Locate every Plasmodium parasite.
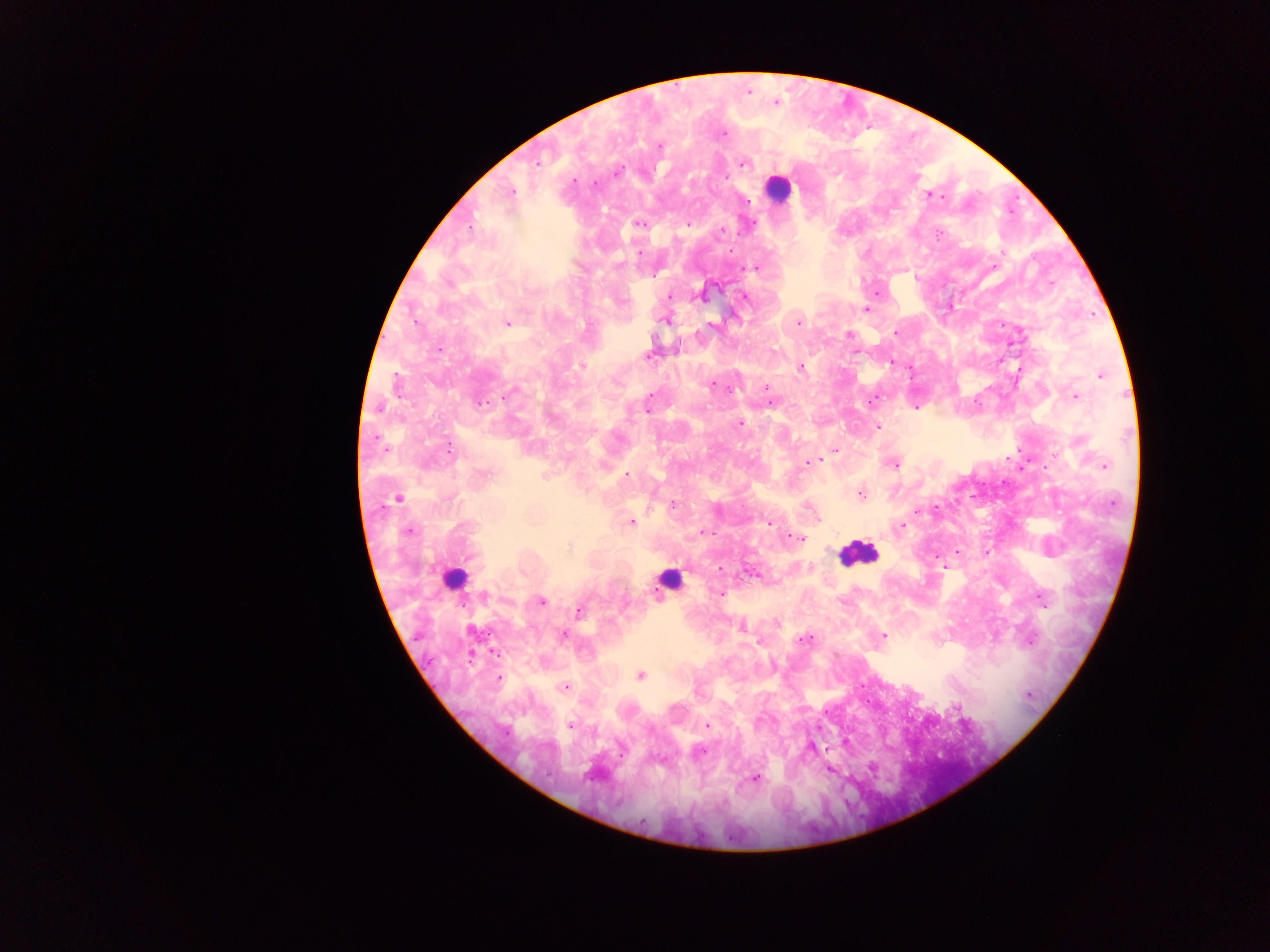

Approximate centers as [x, y] in pixels.
Plasmodium parasites: [776, 102], [723, 133], [660, 146], [538, 163], [743, 163], [617, 171], [575, 180], [593, 184], [511, 191], [930, 195], [937, 197], [748, 201], [639, 223], [688, 224], [470, 227], [721, 230], [938, 233], [639, 252], [755, 268], [1051, 282], [700, 295], [669, 296], [744, 297], [866, 309], [664, 320], [507, 323], [798, 323], [712, 326], [895, 333], [850, 334], [439, 349], [855, 352], [647, 356], [891, 362], [582, 366], [800, 367], [1101, 375], [712, 385], [766, 388], [730, 389], [512, 391], [1075, 396], [872, 401], [771, 402], [480, 403], [378, 407], [647, 408], [740, 424], [878, 427], [449, 450], [835, 450], [817, 460], [807, 462], [893, 463], [1104, 466], [626, 475], [543, 476], [860, 493], [397, 500], [673, 504], [918, 512], [631, 522], [768, 524], [901, 525], [408, 531], [705, 532], [798, 538], [945, 566], [721, 569], [753, 573], [720, 593], [484, 596], [1041, 598], [542, 602], [579, 611], [742, 628], [563, 635], [882, 636], [804, 639], [1030, 642], [495, 653], [640, 675], [500, 678], [565, 686], [1028, 695], [957, 707], [707, 725], [570, 726], [701, 751], [830, 770], [755, 778].

Summary:
  - Leukocyte locations: [778, 188], [858, 553], [454, 579], [669, 579]
  - Preparation: thick blood film
  - Image size: 1270×952 pixels
  - Field of view: single
  - Capture: mobile-phone photograph through a microscope
  - Country: Ghana